Assess this cell for malaria.
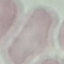

Uninfected.

Acquired by smartphone through the microscope eyepiece. Thin smear of blood. Giemsa stain. Automatically extracted cell patch, resized to 64 × 64 pixels.